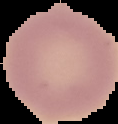

Summary:
  - Image size: 118×124 pixels
  - Image type: cell region segmented out of the field of view; surrounding area masked to black
  - Result: no Plasmodium parasites seen
  - Preparation: thin blood smear